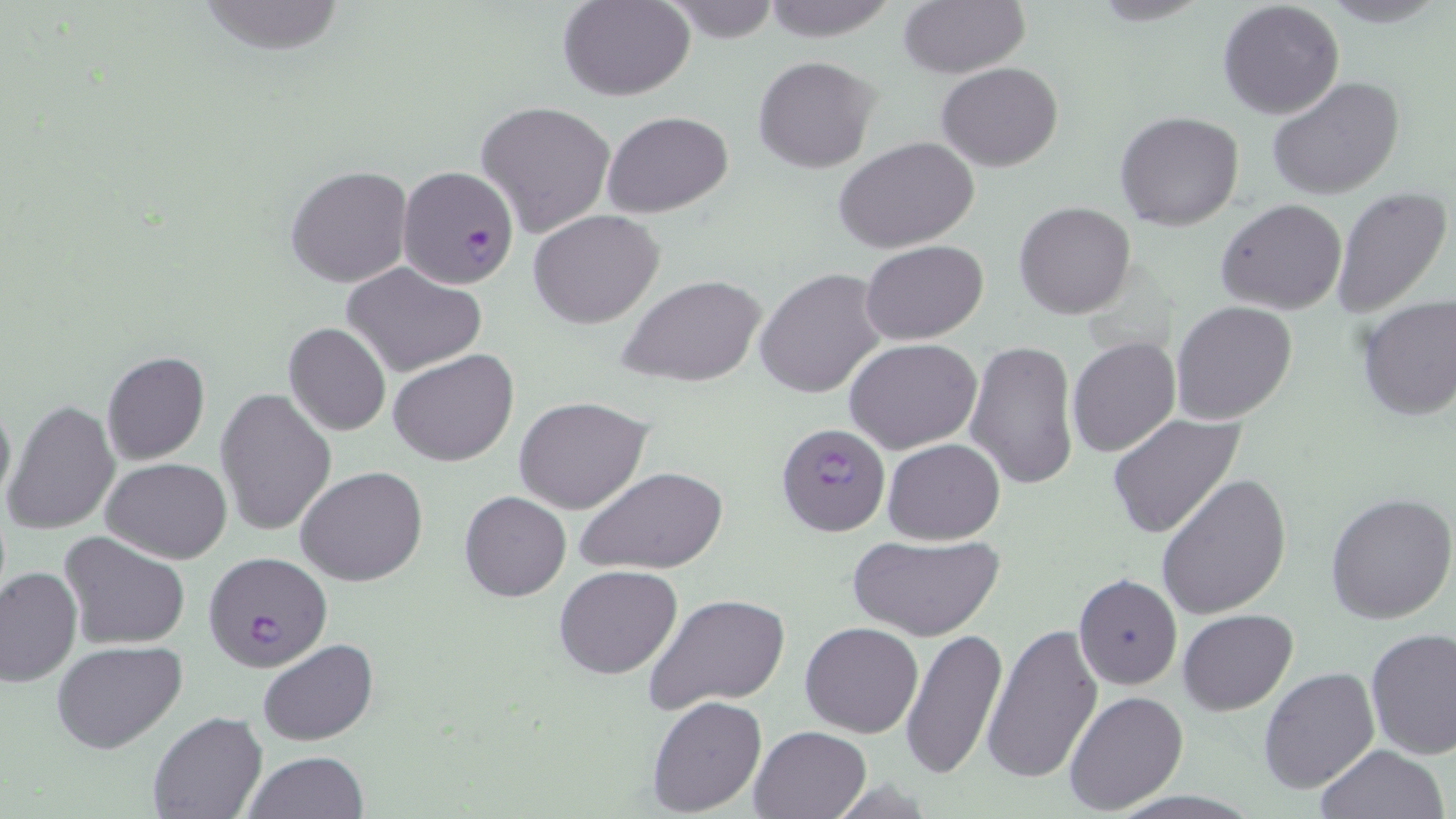
Approximate bounding boxes as [x1, y1, x2, y2] in pixels. Plasmodium falciparum-infected red blood cell locations: [397, 164, 521, 289], [775, 421, 889, 536], [203, 551, 333, 672]. Uninfected red blood cell locations: [559, 0, 696, 100], [898, 0, 1029, 78], [757, 1, 903, 42], [1217, 1, 1345, 118], [753, 57, 879, 173], [936, 63, 1063, 171], [1267, 77, 1407, 203], [476, 100, 616, 237], [603, 110, 732, 218], [1115, 110, 1244, 230], [834, 135, 981, 255], [285, 164, 414, 288], [1330, 187, 1451, 318], [1216, 199, 1347, 315], [1013, 202, 1137, 320], [530, 208, 665, 329], [861, 241, 986, 346], [343, 263, 487, 377], [755, 268, 888, 400], [618, 275, 766, 388], [1356, 294, 1456, 422], [1170, 301, 1298, 427], [284, 321, 391, 436], [1067, 336, 1181, 458], [846, 337, 983, 453], [966, 339, 1080, 492], [389, 349, 519, 467], [101, 351, 211, 464], [215, 388, 337, 536], [0, 390, 15, 513], [515, 396, 654, 514], [5, 399, 120, 537], [1107, 413, 1249, 541], [534, 421, 701, 553], [882, 439, 1005, 545], [102, 458, 231, 563], [296, 465, 428, 587], [573, 465, 730, 574], [1157, 473, 1292, 617], [459, 490, 571, 601], [1325, 493, 1456, 625], [59, 531, 189, 649], [847, 533, 1004, 641], [0, 565, 81, 686], [554, 566, 682, 680], [1072, 572, 1183, 689], [645, 593, 788, 713], [1177, 609, 1297, 714], [800, 621, 923, 738], [983, 621, 1104, 785], [899, 627, 1008, 779], [1365, 627, 1456, 759], [260, 639, 379, 746], [51, 640, 187, 753], [1258, 666, 1380, 793], [1061, 689, 1187, 814], [647, 695, 768, 817], [149, 711, 268, 819], [748, 724, 873, 818], [1314, 744, 1449, 819], [244, 751, 367, 819]. Slide-level diagnosis: Plasmodium falciparum. Light microscopy. May-Grünwald-Giemsa-stained preparation. Image is 1456×819 pixels. Thin blood smear. Captured at 1000x magnification. One field of a larger specimen.